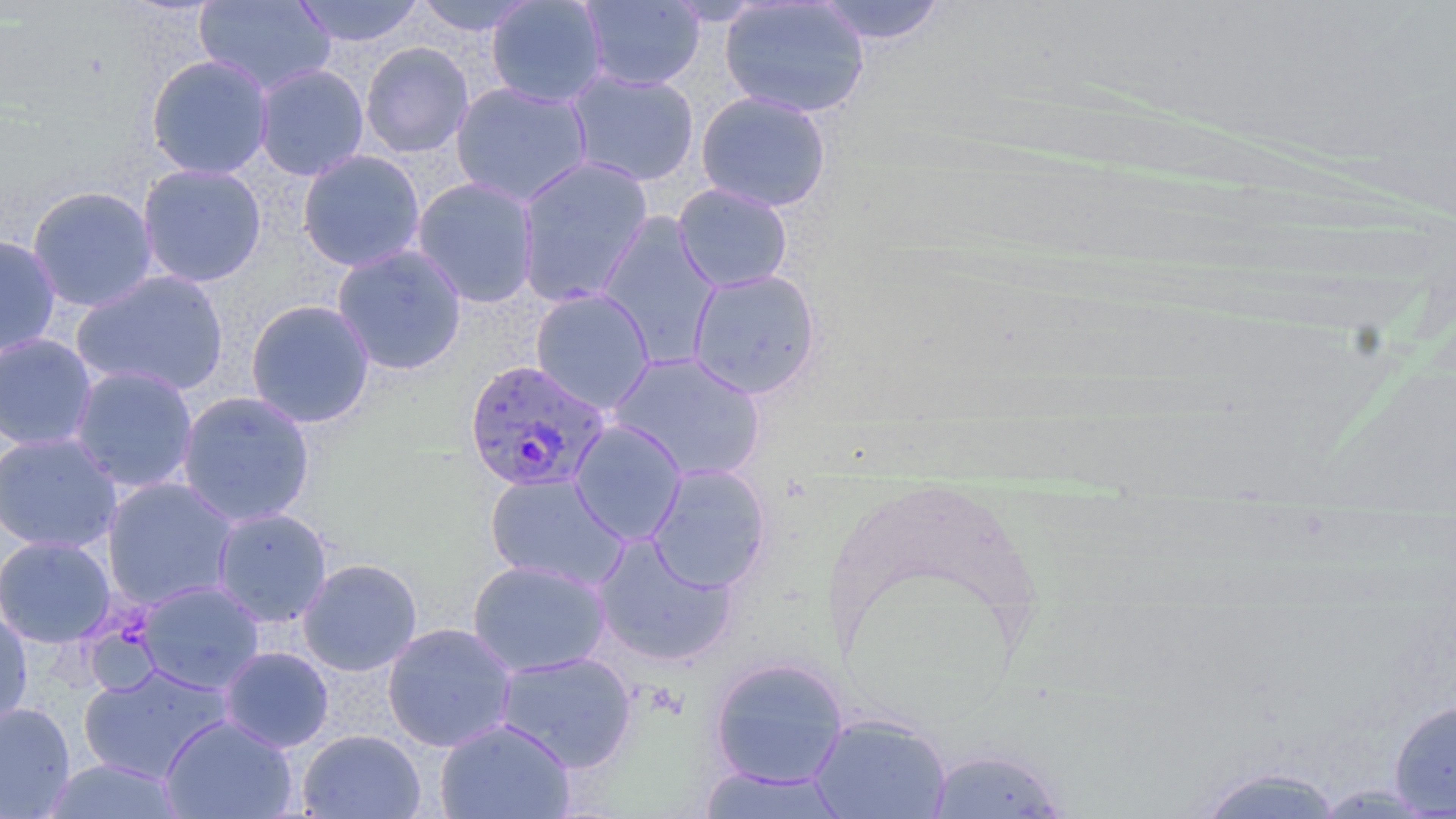
slide-level diagnosis = Plasmodium falciparum
image size = 1456×819 pixels
modality = optical microscopy
Plasmodium falciparum-infected red blood cell locations = approximate bounding boxes as (x1,y1)-(x2,y2) corner pairs in pixels: (463,358)-(610,493)
uninfected red blood cell locations = approximate bounding boxes as (x1,y1)-(x2,y2) corner pairs in pixels: (194,0)-(336,95), (291,0)-(425,47), (412,0)-(541,36), (486,0)-(608,108), (579,0)-(705,91), (814,0)-(947,45), (720,1)-(870,119), (361,41)-(474,158), (145,53)-(274,180), (253,63)-(369,181), (566,69)-(700,187), (566,80)-(838,194), (450,81)-(593,207), (695,90)-(832,213), (297,149)-(426,272), (515,156)-(653,307), (137,163)-(267,288), (411,177)-(540,308), (673,183)-(793,292), (26,185)-(159,312), (596,213)-(720,367), (0,234)-(61,357), (331,243)-(467,376), (687,268)-(821,399), (70,270)-(230,397), (530,287)-(655,414), (244,299)-(375,428), (0,333)-(99,451), (608,351)-(767,482), (68,365)-(199,494), (176,390)-(316,527), (569,419)-(687,546), (0,431)-(123,553), (646,464)-(771,592), (484,472)-(628,590), (101,477)-(240,610), (211,507)-(332,628), (591,533)-(738,668), (0,535)-(116,648), (297,557)-(423,676), (467,559)-(611,677), (137,581)-(265,694), (0,607)-(33,731), (382,622)-(518,752), (219,646)-(334,752), (495,650)-(637,773), (708,655)-(849,789), (78,664)-(233,784), (1388,698)-(1456,817), (0,702)-(76,818), (809,713)-(951,818), (160,714)-(298,818), (434,717)-(577,819), (298,729)-(425,819), (926,745)-(1071,818), (47,759)-(183,818), (1189,764)-(1347,818), (695,766)-(852,817)
magnification = 1000x
preparation = thin blood smear
stain = May-Grünwald-Giemsa
field of view = single